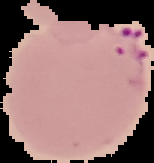

image size = 154×163 pixels
preparation = thin blood film
image type = segmented cell region on a black background
result = Plasmodium parasites detected